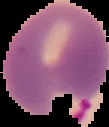

{
  "preparation": "thin blood film",
  "image_size": "109×127 pixels",
  "image_type": "segmented cell region with the area outside set to black",
  "result": "malaria parasites identified"
}